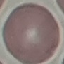
{
  "malaria_status": "uninfected",
  "image_type": "cell patch, automatically extracted from a larger field of view and resized to 64 × 64 pixels",
  "stain": "Giemsa",
  "preparation": "thin smear",
  "capture": "smartphone camera at the microscope eyepiece"
}